State the blood parasite species.
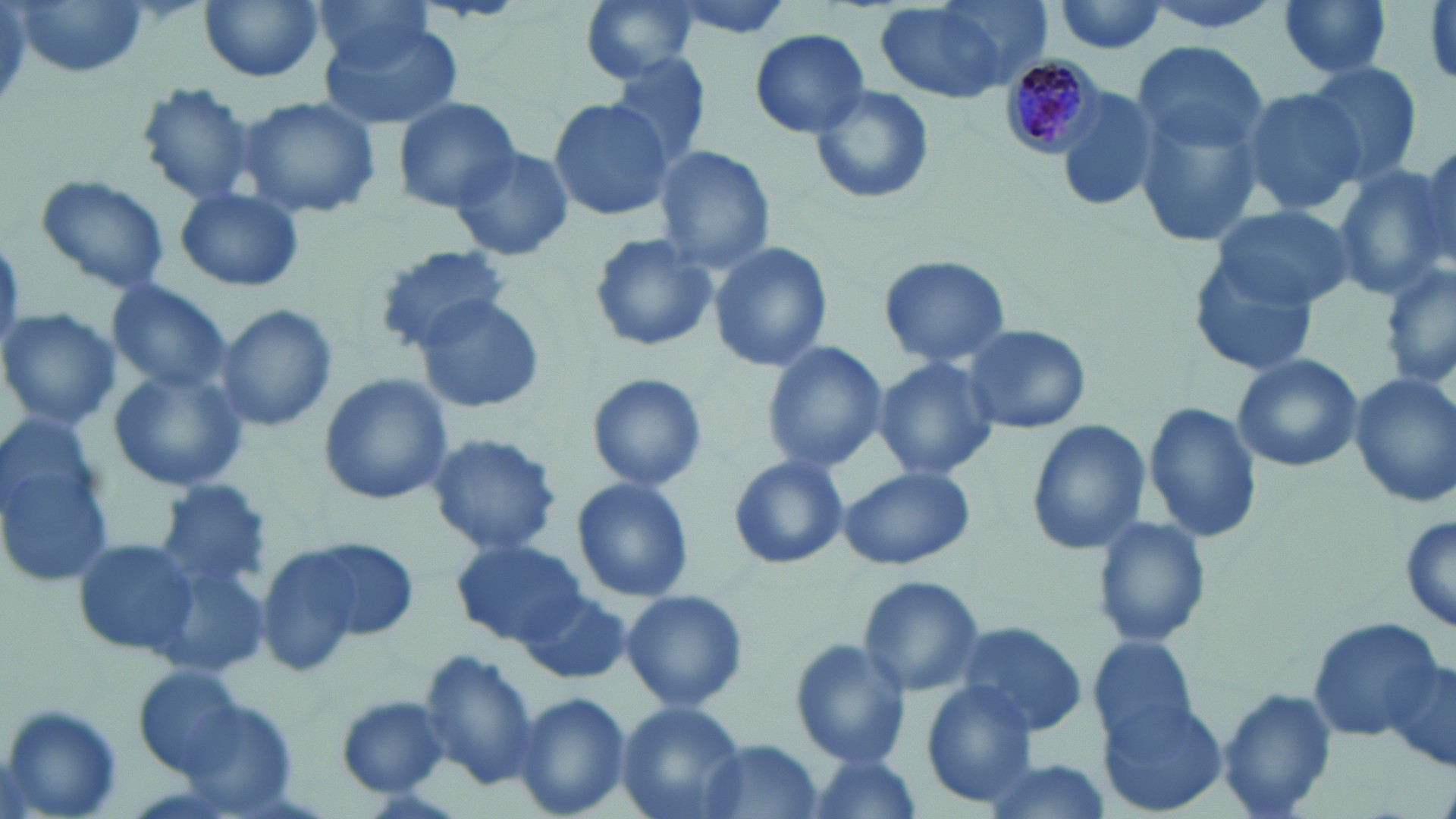

Plasmodium malariae.

Approximate bounding boxes as (x1,y1)-(x2,y2) corner pairs in pixels. Uninfected red blood cell locations: (8,0)-(154,80), (197,0)-(326,83), (313,0)-(437,76), (579,0)-(700,83), (658,0)-(804,39), (873,0)-(1041,104), (1278,0)-(1393,82), (1051,1)-(1172,55), (319,19)-(463,130), (749,28)-(872,138), (1132,40)-(1269,159), (606,51)-(714,169), (1303,62)-(1423,186), (1129,81)-(1269,257), (135,83)-(261,207), (806,84)-(935,205), (1053,84)-(1165,214), (1237,87)-(1362,215), (238,95)-(381,218), (394,97)-(522,211), (549,97)-(672,222), (1412,141)-(1455,268), (448,144)-(575,262), (654,145)-(775,274), (1331,163)-(1451,295), (32,172)-(172,298), (174,186)-(304,294), (1209,205)-(1355,309), (587,232)-(717,352), (710,241)-(833,372), (371,244)-(510,352), (1185,251)-(1322,378), (878,254)-(1011,368), (1380,262)-(1456,392), (106,281)-(235,398), (414,293)-(549,413), (215,305)-(337,434), (0,309)-(120,430), (959,322)-(1092,434), (762,343)-(886,473), (1231,353)-(1364,471), (873,357)-(999,482), (105,366)-(249,493), (585,371)-(706,493), (1348,372)-(1456,507), (320,373)-(452,504), (1143,402)-(1263,545), (0,414)-(114,591), (1025,420)-(1153,556), (425,433)-(562,558), (727,455)-(848,569), (833,468)-(976,570), (152,477)-(273,592), (571,478)-(694,603), (1399,511)-(1455,638), (1093,515)-(1212,648), (73,537)-(199,658), (276,537)-(422,655), (452,539)-(589,646), (147,560)-(270,676), (855,574)-(986,697), (520,588)-(631,687), (619,588)-(747,711), (1306,615)-(1447,743), (948,619)-(1089,738), (1089,635)-(1202,745), (787,638)-(911,768), (1383,648)-(1455,774), (417,651)-(541,790), (137,666)-(250,775), (919,683)-(1038,807), (1216,685)-(1339,819), (511,692)-(631,818), (1097,692)-(1231,818), (335,696)-(448,798), (616,701)-(746,819), (1,705)-(122,817), (694,739)-(827,819), (802,752)-(919,819), (974,754)-(1112,819). Plasmodium malariae-infected red blood cell locations: (1000,57)-(1101,156). Single field of view. May-Grünwald-Giemsa-stained preparation. Light microscopy. Image is 1456×819 pixels. Thin blood film. Captured at 1000x magnification.